Assess this cell for malaria.
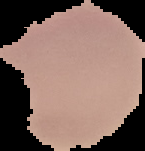

Uninfected.

image_size: 145×151 pixels
preparation: thin blood film
image_type: segmented cell region on a black background